Assess this cell for malaria.
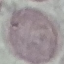
Uninfected.

Summary:
  - Preparation: thin smear
  - Capture: smartphone camera at the microscope eyepiece
  - Image type: automatically extracted cell patch, resized to 64 × 64 pixels
  - Stain: Giemsa